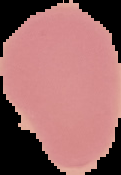
preparation = thin blood smear
image type = segmented cell region on a black background
image size = 121×175 pixels
result = negative for malaria parasites